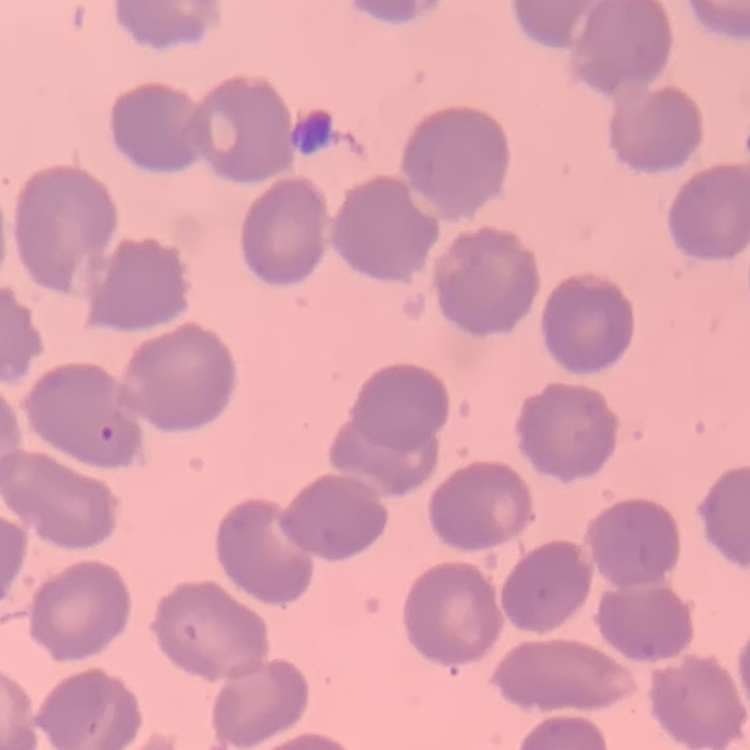
red blood cell morphology = no rouleaux formation
preparation = thin blood smear
image type = square crop of a larger photomicrograph
stain = Field's or Giemsa